Locate white blood cells.
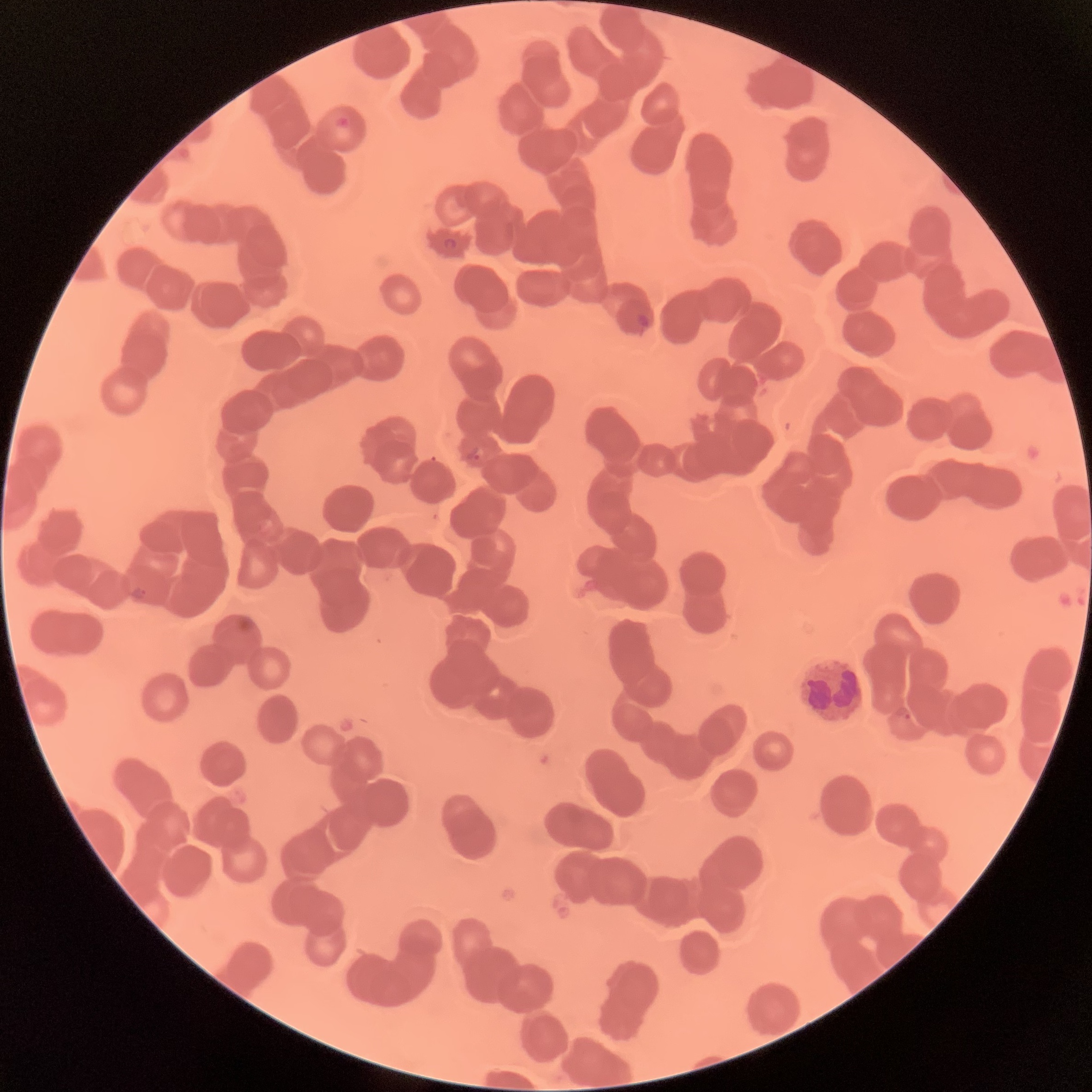

Approximate bounding boxes as (x1, y1, x2, y2) in pixels.
White blood cells: (797, 657, 865, 723).

Plasmodium parasite locations: (333, 116, 351, 130), (443, 238, 459, 250), (635, 313, 654, 330), (467, 448, 485, 463), (129, 586, 147, 600), (902, 711, 912, 720). Optical microscopy. Image is 1092×1092 pixels. The red blood cells show rouleaux formation. Thin blood film.